Identify the blood parasite species.
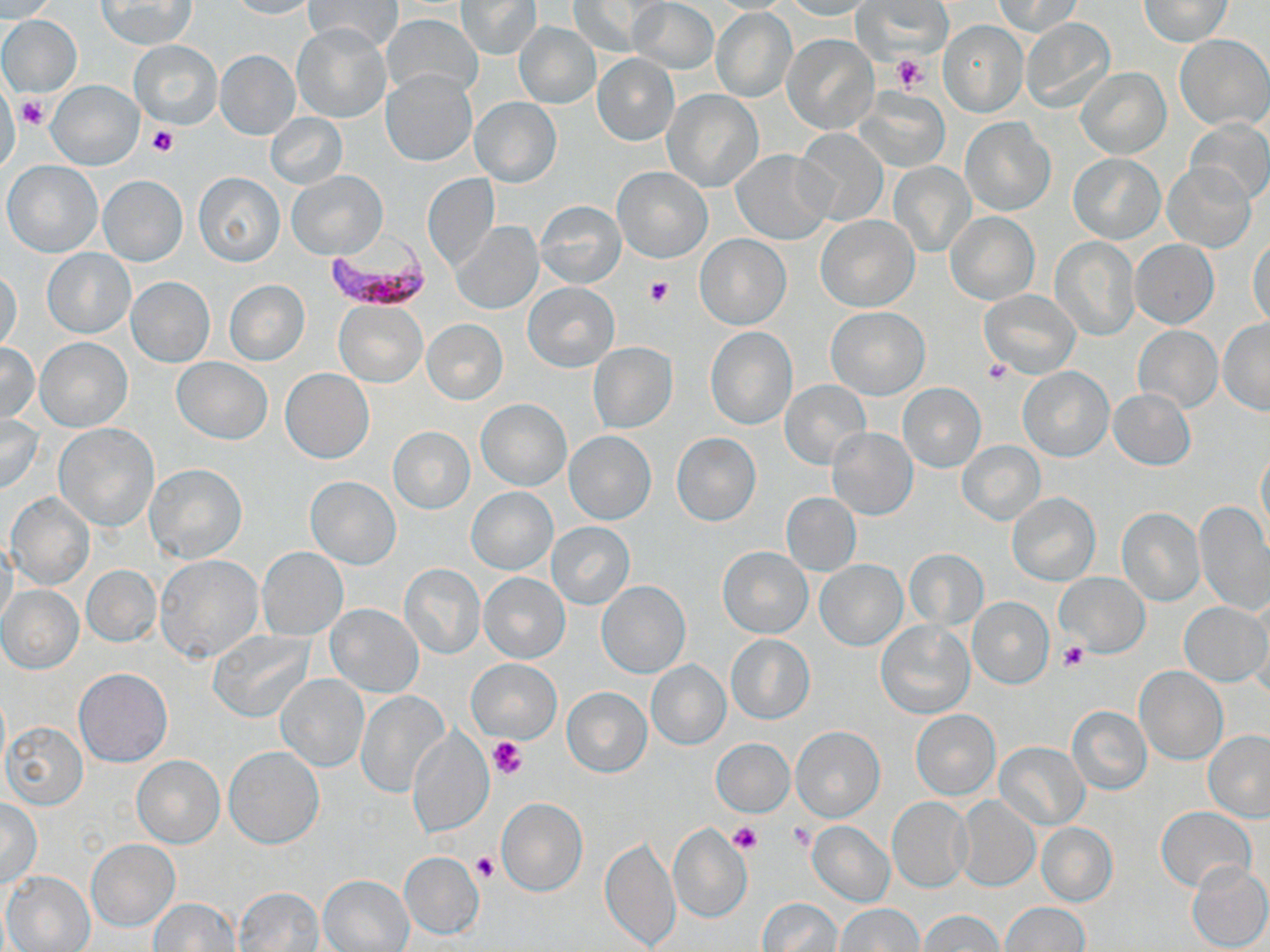
Plasmodium falciparum.

Approximate bounding boxes as named x1/y1/x2/y2 corners in pixels. Platelet locations: (x1=892, y1=55, x2=927, y2=94), (x1=17, y1=94, x2=50, y2=131), (x1=146, y1=123, x2=177, y2=156), (x1=645, y1=276, x2=675, y2=304), (x1=982, y1=358, x2=1013, y2=384), (x1=1060, y1=641, x2=1090, y2=671), (x1=488, y1=737, x2=525, y2=778), (x1=728, y1=823, x2=762, y2=853), (x1=790, y1=823, x2=817, y2=851), (x1=472, y1=853, x2=499, y2=882). Plasmodium falciparum-infected red blood cell locations: (x1=322, y1=234, x2=433, y2=311). Uninfected red blood cell locations: (x1=2, y1=0, x2=54, y2=20), (x1=96, y1=0, x2=197, y2=49), (x1=227, y1=0, x2=318, y2=19), (x1=458, y1=0, x2=541, y2=58), (x1=629, y1=0, x2=718, y2=74), (x1=706, y1=0, x2=799, y2=13), (x1=782, y1=0, x2=878, y2=20), (x1=854, y1=0, x2=949, y2=58), (x1=992, y1=0, x2=1083, y2=36), (x1=1140, y1=0, x2=1233, y2=46), (x1=304, y1=1, x2=402, y2=53), (x1=567, y1=2, x2=660, y2=57), (x1=711, y1=7, x2=797, y2=102), (x1=697, y1=10, x2=784, y2=173), (x1=0, y1=14, x2=82, y2=97), (x1=384, y1=14, x2=481, y2=101), (x1=1023, y1=18, x2=1117, y2=112), (x1=938, y1=20, x2=1027, y2=117), (x1=514, y1=22, x2=600, y2=107), (x1=293, y1=24, x2=391, y2=121), (x1=1176, y1=34, x2=1270, y2=130), (x1=783, y1=35, x2=877, y2=133), (x1=130, y1=39, x2=222, y2=129), (x1=216, y1=51, x2=300, y2=138), (x1=591, y1=53, x2=679, y2=146), (x1=1075, y1=68, x2=1170, y2=159), (x1=382, y1=69, x2=477, y2=166), (x1=47, y1=81, x2=142, y2=170), (x1=0, y1=85, x2=21, y2=173), (x1=664, y1=89, x2=762, y2=192), (x1=856, y1=89, x2=950, y2=171), (x1=469, y1=96, x2=561, y2=187), (x1=265, y1=114, x2=347, y2=189), (x1=961, y1=117, x2=1054, y2=216), (x1=1187, y1=118, x2=1270, y2=206), (x1=795, y1=128, x2=888, y2=226), (x1=731, y1=151, x2=832, y2=245), (x1=1068, y1=153, x2=1164, y2=243), (x1=3, y1=161, x2=103, y2=257), (x1=889, y1=161, x2=975, y2=255), (x1=1164, y1=163, x2=1255, y2=251), (x1=611, y1=166, x2=713, y2=263), (x1=287, y1=169, x2=387, y2=259), (x1=194, y1=172, x2=284, y2=266), (x1=422, y1=173, x2=498, y2=272), (x1=98, y1=176, x2=187, y2=266), (x1=537, y1=200, x2=626, y2=288), (x1=946, y1=212, x2=1038, y2=305), (x1=815, y1=215, x2=918, y2=312), (x1=452, y1=222, x2=541, y2=314), (x1=1248, y1=234, x2=1270, y2=328), (x1=696, y1=235, x2=790, y2=329), (x1=1050, y1=236, x2=1140, y2=340), (x1=1129, y1=240, x2=1219, y2=329), (x1=42, y1=249, x2=135, y2=338), (x1=0, y1=269, x2=23, y2=354), (x1=127, y1=276, x2=214, y2=366), (x1=224, y1=279, x2=309, y2=365), (x1=522, y1=281, x2=619, y2=373), (x1=981, y1=290, x2=1080, y2=378), (x1=334, y1=300, x2=427, y2=387), (x1=826, y1=307, x2=929, y2=399), (x1=1217, y1=318, x2=1270, y2=415), (x1=422, y1=320, x2=507, y2=404), (x1=1133, y1=326, x2=1222, y2=413), (x1=706, y1=327, x2=797, y2=429), (x1=37, y1=337, x2=131, y2=431), (x1=0, y1=342, x2=40, y2=428), (x1=588, y1=342, x2=678, y2=434), (x1=172, y1=357, x2=272, y2=445), (x1=1019, y1=367, x2=1113, y2=460), (x1=279, y1=369, x2=374, y2=463), (x1=780, y1=379, x2=870, y2=469), (x1=898, y1=383, x2=984, y2=473), (x1=1108, y1=388, x2=1195, y2=469), (x1=476, y1=399, x2=570, y2=490), (x1=0, y1=413, x2=44, y2=494), (x1=54, y1=423, x2=158, y2=531), (x1=388, y1=426, x2=475, y2=514), (x1=826, y1=429, x2=917, y2=520), (x1=564, y1=431, x2=656, y2=525), (x1=672, y1=433, x2=761, y2=525), (x1=958, y1=440, x2=1045, y2=524), (x1=1256, y1=446, x2=1269, y2=539), (x1=145, y1=463, x2=247, y2=563), (x1=306, y1=476, x2=400, y2=570), (x1=467, y1=487, x2=556, y2=574), (x1=1006, y1=492, x2=1101, y2=585), (x1=781, y1=493, x2=861, y2=575), (x1=6, y1=494, x2=95, y2=590), (x1=1194, y1=501, x2=1269, y2=616), (x1=1116, y1=508, x2=1204, y2=605), (x1=547, y1=522, x2=635, y2=609), (x1=1, y1=538, x2=18, y2=633), (x1=258, y1=546, x2=348, y2=639), (x1=718, y1=547, x2=813, y2=638), (x1=903, y1=549, x2=990, y2=629), (x1=156, y1=555, x2=263, y2=663), (x1=815, y1=560, x2=907, y2=651), (x1=399, y1=563, x2=485, y2=659), (x1=82, y1=566, x2=161, y2=647), (x1=480, y1=573, x2=569, y2=663), (x1=1056, y1=574, x2=1148, y2=657), (x1=0, y1=578, x2=158, y2=659), (x1=597, y1=581, x2=689, y2=678), (x1=1, y1=586, x2=83, y2=673), (x1=1249, y1=593, x2=1270, y2=696), (x1=967, y1=595, x2=1054, y2=689), (x1=1179, y1=601, x2=1269, y2=687), (x1=326, y1=604, x2=423, y2=698), (x1=877, y1=621, x2=974, y2=719), (x1=207, y1=629, x2=315, y2=722), (x1=725, y1=633, x2=814, y2=724), (x1=466, y1=658, x2=562, y2=743), (x1=646, y1=659, x2=730, y2=749), (x1=1134, y1=667, x2=1227, y2=765), (x1=74, y1=668, x2=172, y2=767), (x1=277, y1=674, x2=368, y2=770), (x1=561, y1=686, x2=652, y2=778), (x1=356, y1=690, x2=447, y2=795), (x1=1065, y1=705, x2=1151, y2=795), (x1=911, y1=709, x2=1001, y2=800), (x1=0, y1=721, x2=87, y2=810), (x1=790, y1=726, x2=884, y2=822), (x1=408, y1=730, x2=492, y2=837), (x1=1204, y1=730, x2=1270, y2=822), (x1=710, y1=738, x2=795, y2=816), (x1=996, y1=741, x2=1089, y2=830), (x1=225, y1=747, x2=323, y2=848), (x1=133, y1=756, x2=224, y2=847), (x1=497, y1=797, x2=588, y2=895), (x1=956, y1=797, x2=1038, y2=891), (x1=887, y1=798, x2=971, y2=892), (x1=1, y1=799, x2=42, y2=889), (x1=1156, y1=806, x2=1256, y2=893), (x1=806, y1=821, x2=895, y2=906), (x1=1036, y1=822, x2=1117, y2=907), (x1=668, y1=824, x2=751, y2=924), (x1=601, y1=837, x2=680, y2=950), (x1=87, y1=839, x2=179, y2=930), (x1=399, y1=851, x2=483, y2=939), (x1=1185, y1=862, x2=1270, y2=951), (x1=3, y1=871, x2=96, y2=952), (x1=319, y1=874, x2=415, y2=952), (x1=235, y1=887, x2=325, y2=952), (x1=149, y1=898, x2=239, y2=950), (x1=756, y1=898, x2=843, y2=951), (x1=999, y1=901, x2=1089, y2=952), (x1=835, y1=903, x2=926, y2=951), (x1=920, y1=910, x2=1005, y2=951). Image is 1270×952 pixels. May-Grünwald-Giemsa stain. One field of a larger specimen. Optical microscopy. 1000x magnification. Thin blood film.